Give the position of every Plasmodium parasite visible.
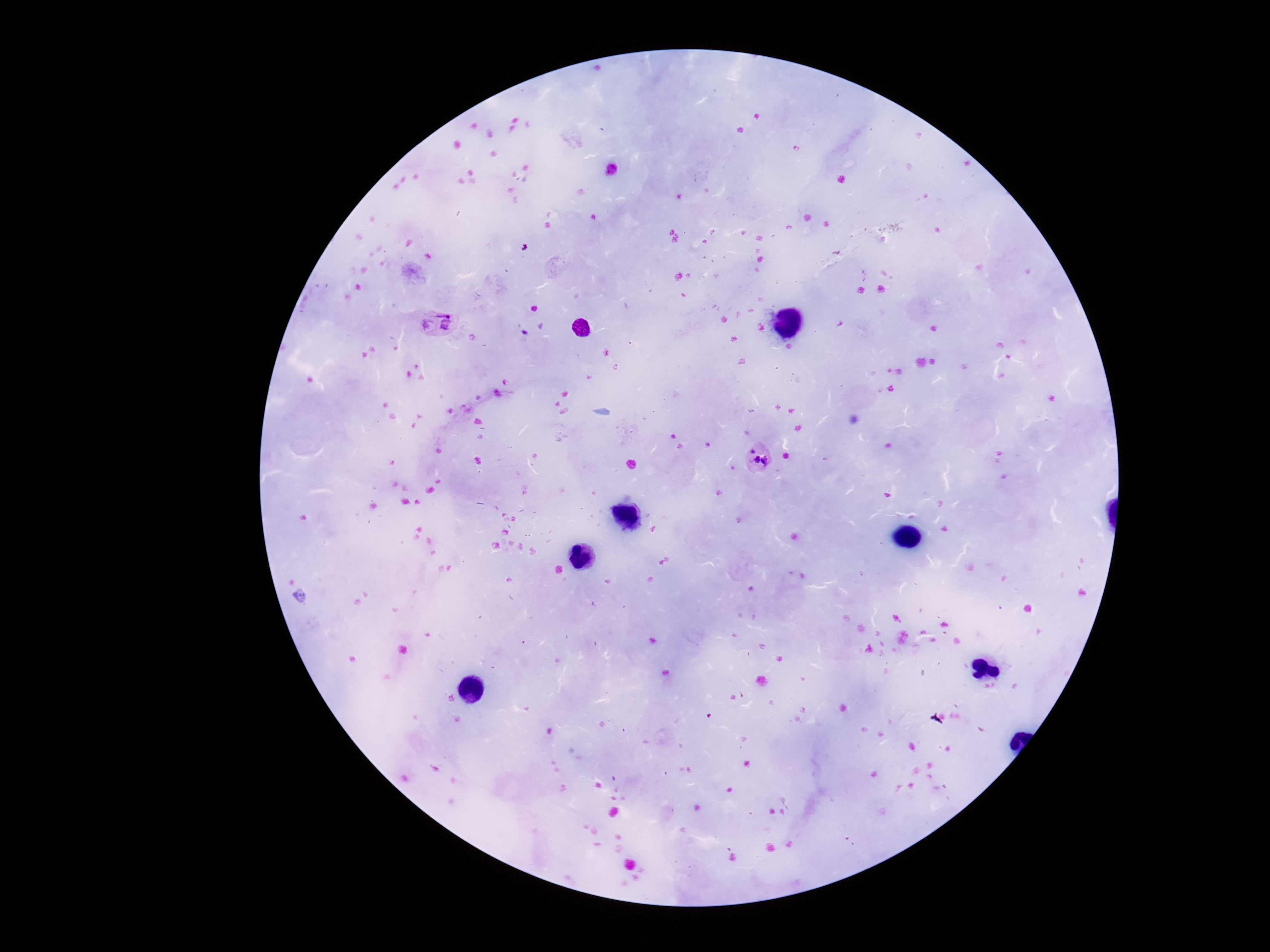
Approximate centers as (x, y) in pixels.
Plasmodium parasites: (435, 323), (759, 457).

Summary:
  - Image size: 1270×952 pixels
  - Field of view: one from this slide
  - Stain: Giemsa
  - Patient malaria status: positive
  - Preparation: thick blood smear
  - Magnification: 100x
  - Capture: smartphone camera through the microscope eyepiece